Give the extent of all Plasmodium ovale-infected red blood cells.
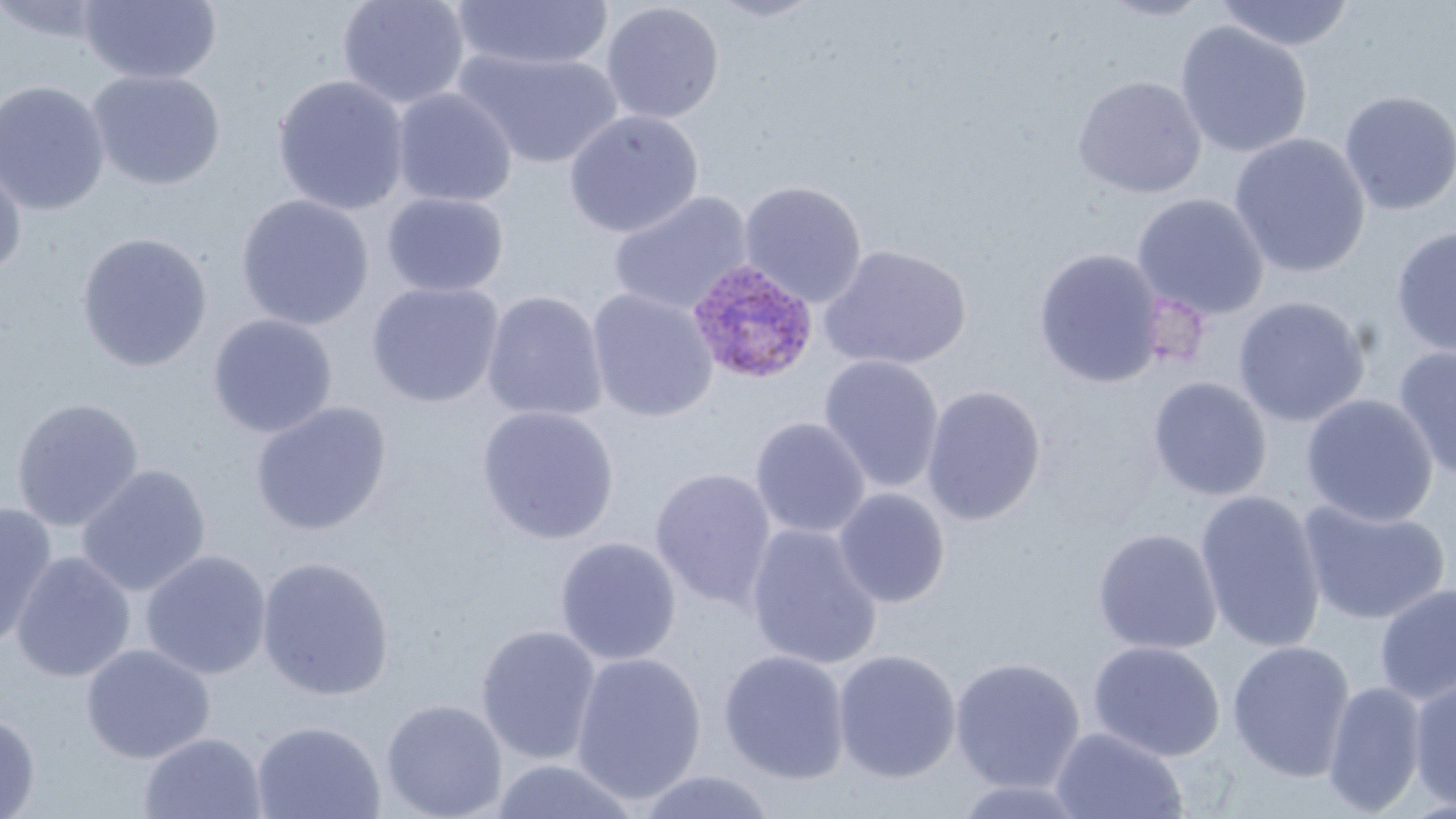

Approximate bounding boxes as named x1/y1/x2/y2 corners in pixels.
Plasmodium ovale-infected red blood cells: (x1=686, y1=257, x2=819, y2=385).

slide-level diagnosis = Plasmodium ovale
field of view = single
image size = 1456×819 pixels
uninfected red blood cell locations = approximate bounding boxes as named x1/y1/x2/y2 corners in pixels: (x1=79, y1=0, x2=222, y2=85), (x1=337, y1=0, x2=470, y2=109), (x1=706, y1=0, x2=825, y2=22), (x1=1096, y1=0, x2=1215, y2=23), (x1=1215, y1=0, x2=1355, y2=52), (x1=0, y1=1, x2=115, y2=43), (x1=451, y1=1, x2=613, y2=72), (x1=600, y1=2, x2=724, y2=124), (x1=1174, y1=20, x2=1313, y2=158), (x1=454, y1=48, x2=626, y2=170), (x1=88, y1=69, x2=226, y2=190), (x1=271, y1=74, x2=410, y2=215), (x1=1072, y1=75, x2=1207, y2=198), (x1=0, y1=80, x2=110, y2=216), (x1=391, y1=87, x2=517, y2=208), (x1=1338, y1=90, x2=1456, y2=215), (x1=563, y1=109, x2=704, y2=238), (x1=1228, y1=132, x2=1371, y2=278), (x1=0, y1=154, x2=27, y2=281), (x1=738, y1=180, x2=868, y2=307), (x1=608, y1=190, x2=754, y2=316), (x1=381, y1=192, x2=509, y2=297), (x1=1132, y1=192, x2=1270, y2=320), (x1=236, y1=194, x2=374, y2=330), (x1=1390, y1=225, x2=1456, y2=358), (x1=76, y1=232, x2=213, y2=372), (x1=819, y1=243, x2=972, y2=371), (x1=1033, y1=248, x2=1166, y2=388), (x1=366, y1=281, x2=505, y2=408), (x1=586, y1=288, x2=719, y2=423), (x1=481, y1=290, x2=609, y2=422), (x1=1232, y1=295, x2=1370, y2=427), (x1=207, y1=313, x2=338, y2=438), (x1=1392, y1=345, x2=1456, y2=484), (x1=817, y1=354, x2=945, y2=493), (x1=1148, y1=376, x2=1272, y2=501), (x1=921, y1=385, x2=1047, y2=526), (x1=1300, y1=394, x2=1438, y2=526), (x1=11, y1=397, x2=145, y2=531), (x1=251, y1=400, x2=392, y2=536), (x1=476, y1=405, x2=620, y2=544), (x1=750, y1=416, x2=871, y2=539), (x1=76, y1=463, x2=212, y2=597), (x1=649, y1=467, x2=777, y2=610), (x1=832, y1=487, x2=951, y2=608), (x1=1195, y1=490, x2=1327, y2=654), (x1=1298, y1=499, x2=1452, y2=625), (x1=0, y1=501, x2=58, y2=649), (x1=745, y1=523, x2=883, y2=670), (x1=1092, y1=528, x2=1223, y2=655), (x1=555, y1=536, x2=682, y2=665), (x1=140, y1=549, x2=272, y2=680), (x1=10, y1=551, x2=136, y2=683), (x1=256, y1=555, x2=396, y2=701), (x1=1373, y1=580, x2=1456, y2=705), (x1=476, y1=624, x2=603, y2=764), (x1=1088, y1=640, x2=1225, y2=762), (x1=1227, y1=640, x2=1356, y2=781), (x1=80, y1=643, x2=215, y2=764), (x1=718, y1=649, x2=851, y2=784), (x1=832, y1=649, x2=962, y2=783), (x1=570, y1=651, x2=707, y2=805), (x1=948, y1=656, x2=1086, y2=792), (x1=1409, y1=676, x2=1456, y2=810), (x1=1322, y1=679, x2=1428, y2=815), (x1=381, y1=698, x2=508, y2=819), (x1=0, y1=712, x2=41, y2=818), (x1=252, y1=719, x2=385, y2=819), (x1=1050, y1=726, x2=1188, y2=819), (x1=138, y1=731, x2=267, y2=819), (x1=488, y1=758, x2=643, y2=818), (x1=633, y1=769, x2=778, y2=818), (x1=949, y1=778, x2=1093, y2=818)
modality = optical microscopy
magnification = 1000x
preparation = thin blood film
stain = May-Grünwald-Giemsa